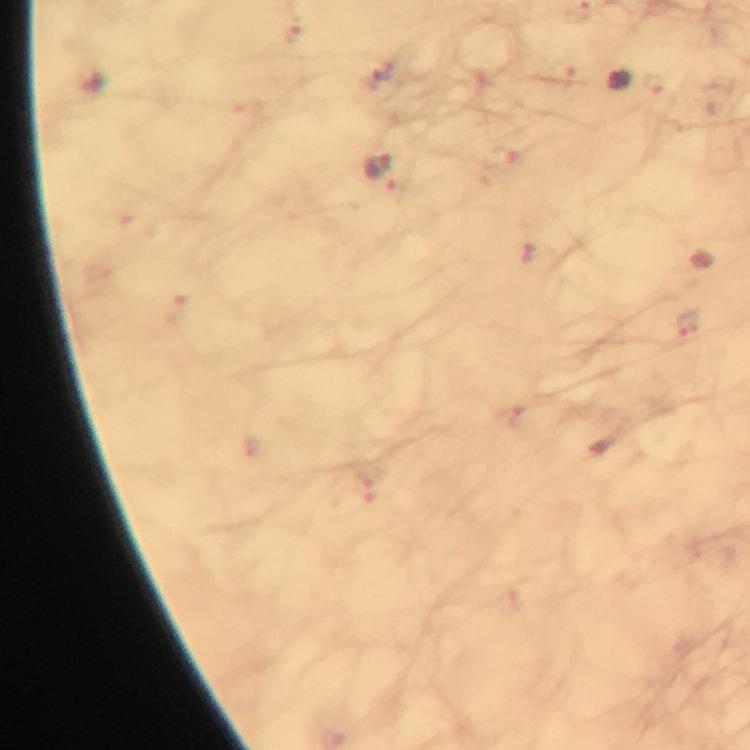

preparation = thick smear
stain = Giemsa
cropped from = a single field of view
capture = smartphone camera through the microscope
context = from a malaria diagnostic workup
image size = 750×750 pixels
immersion oil = applied
Plasmodium parasite locations = approximate centers as {x, y} in pixels: {621, 82}, {377, 165}, {688, 322}
magnification = 100x